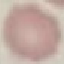

Result: no malaria parasites detected. Cell patch, automatically extracted from a larger field of view and resized to 64 × 64 pixels. Photographed with a smartphone camera at the microscope eyepiece. Giemsa-stained preparation. Thin blood film.